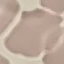
Result: no malaria parasites seen. Photographed with a smartphone camera at the microscope eyepiece. Automatically extracted cell patch, resized to 64 × 64 pixels. Thin blood film. Giemsa-stained preparation.